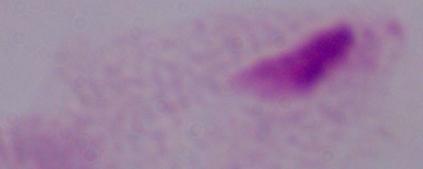
Summary:
  - Identification: trichomonad
  - Modality: photomicrograph
  - Magnification: 1000x